Classify this cell by malaria status.
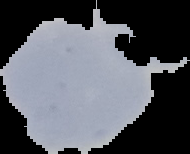
Uninfected.

{
  "image_type": "segmented cell region on a black background",
  "image_size": "190×154 pixels",
  "preparation": "thin blood smear"
}